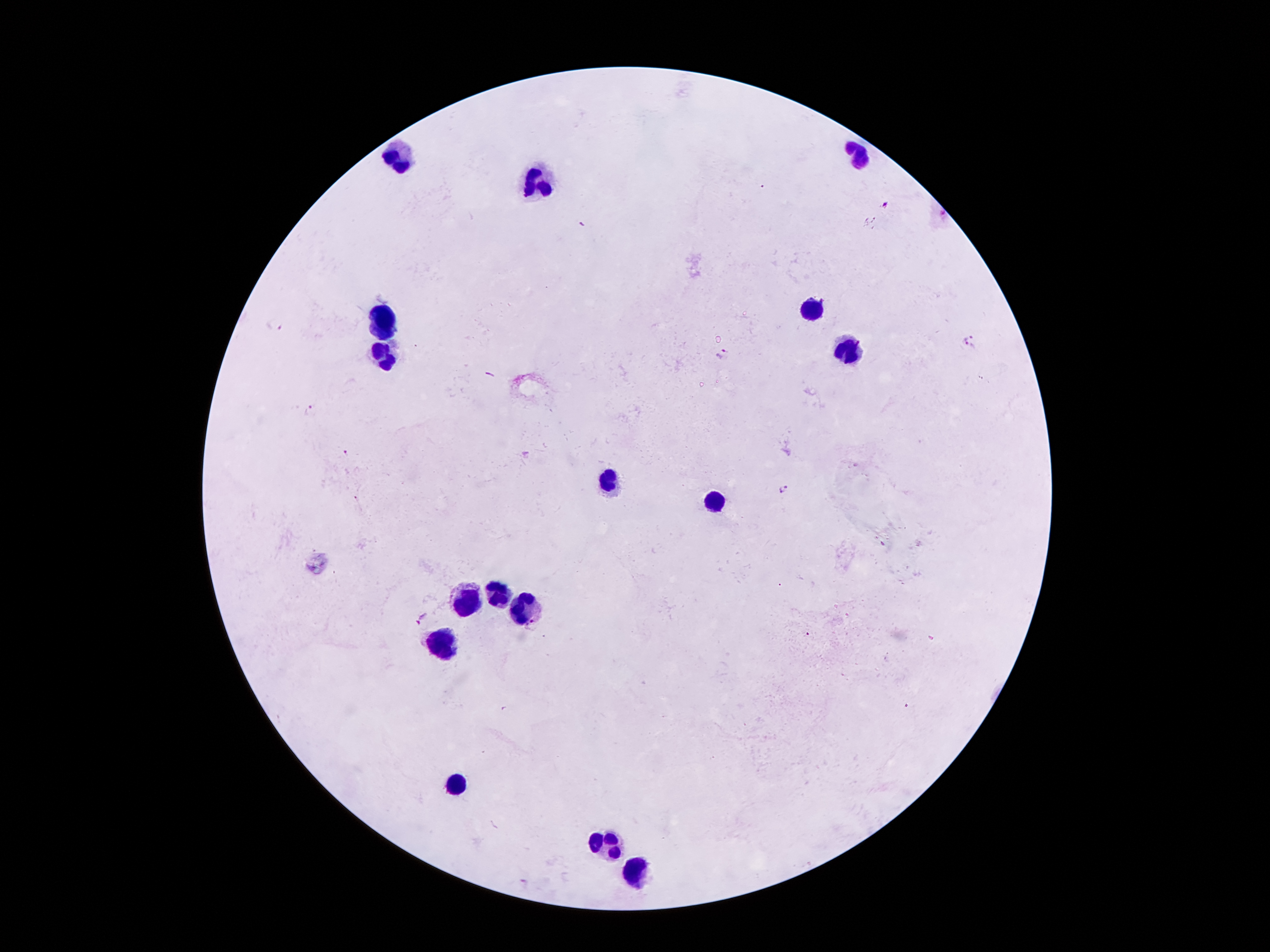
coordinate format = approximate centers as (x, y) in pixels
Plasmodium parasite locations = (886, 202), (943, 214), (275, 323), (969, 336), (968, 348), (722, 352), (312, 410), (346, 452), (784, 488), (356, 498), (422, 620), (531, 625), (806, 634), (525, 882)
leukocyte locations = (860, 152), (397, 157), (540, 184), (812, 309), (385, 318), (850, 352), (385, 359), (608, 477), (716, 500), (469, 593), (499, 595), (523, 604), (439, 647), (455, 786), (607, 845), (635, 874)
capture = smartphone through the microscope eyepiece
preparation = thick peripheral-blood smear
patient malaria status = infected with Plasmodium falciparum
field of view = single
magnification = 100x
image size = 1270×952 pixels
stain = Giemsa